Give the preparation type.
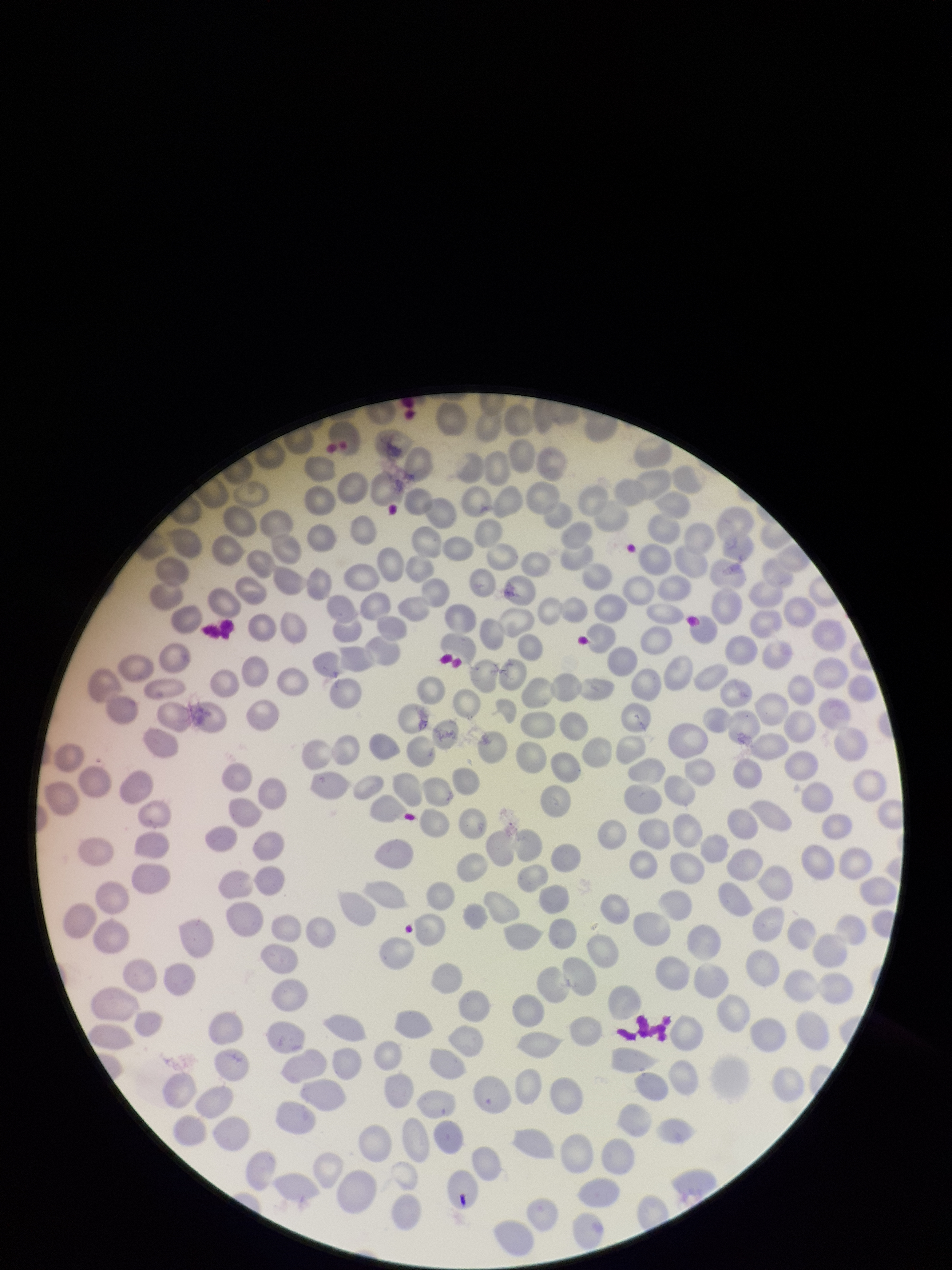

It is a thin blood smear.

Parasitized red blood cells: none detected. Red blood cell count: 276. Patient malaria status: negative. Stained with Giemsa. Parasitized red blood cell count: 0. Image is 952×1270 pixels. One field from this slide. Smartphone photograph taken through the eyepiece of a microscope.